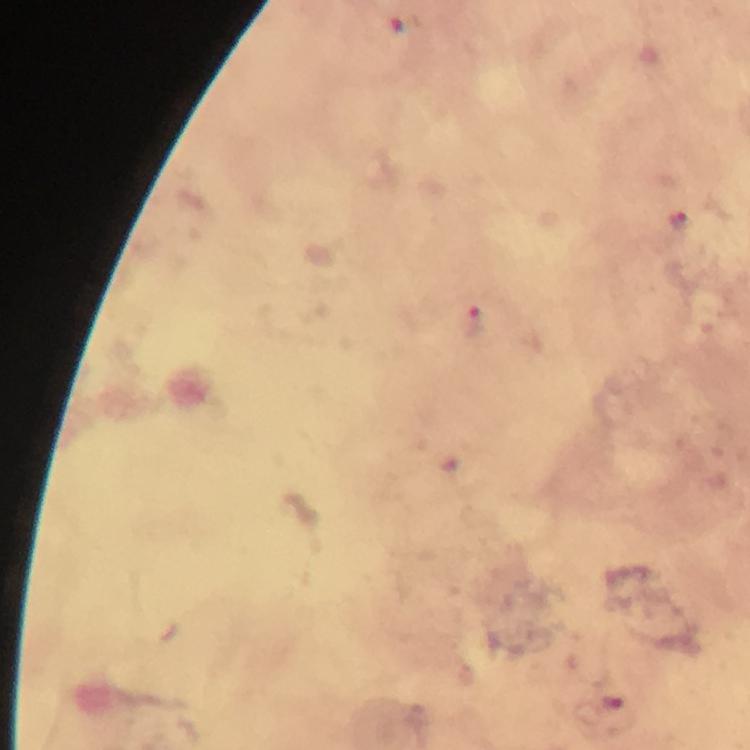

malaria parasite locations = approximate centers as {x, y} in pixels: {679, 221}, {472, 320}
preparation = thick blood smear
context = from a malaria diagnostic workup
image size = 750×750 pixels
stain = Giemsa
immersion oil = applied
magnification = 100x
capture = smartphone mounted on the microscope
cropped from = a single field of view